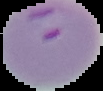

preparation = thin blood film
image type = segmented cell region on a black background
malaria status = parasitized
image size = 103×91 pixels